Assess for malaria.
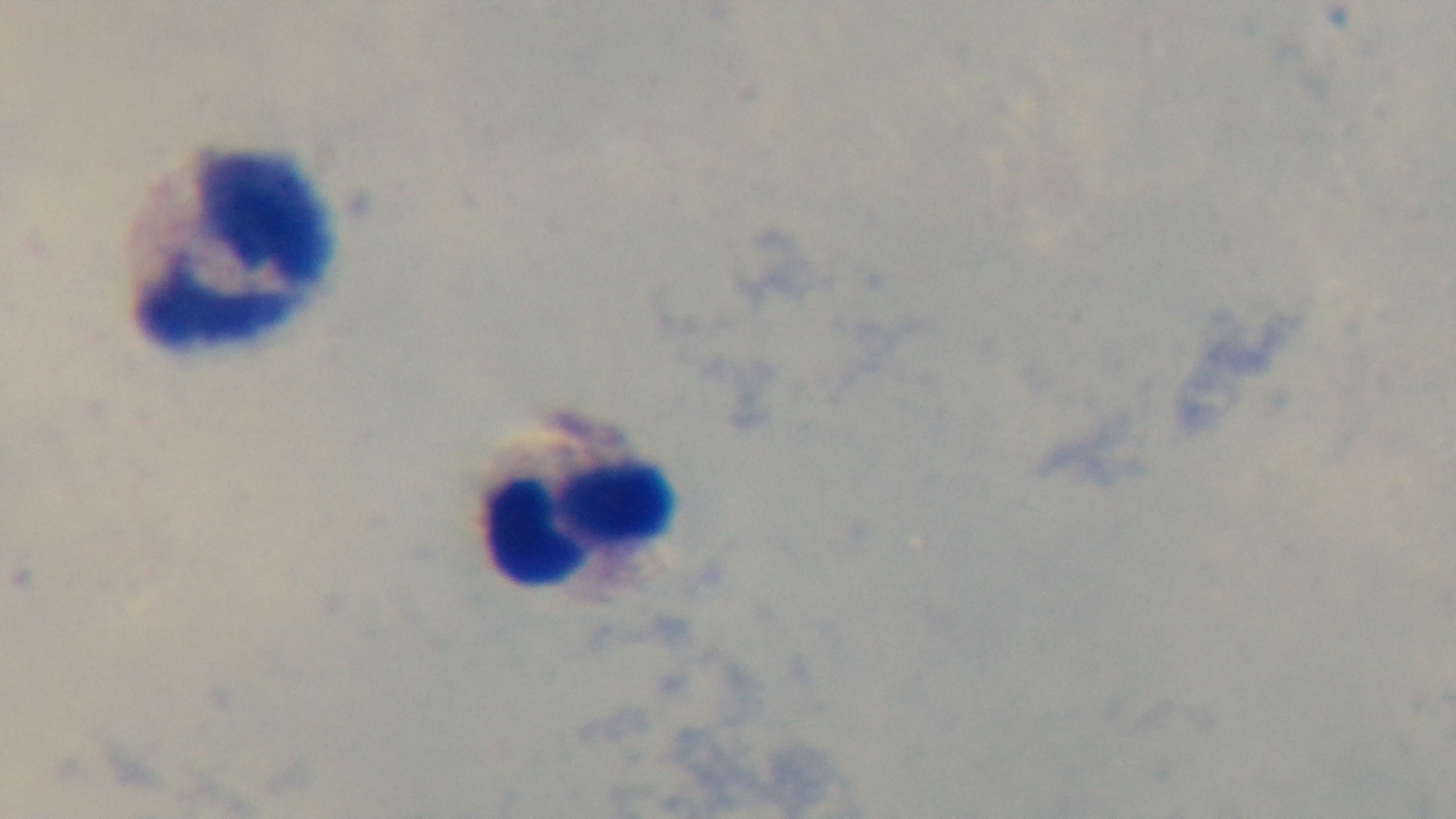

Negative.

Summary:
  - Preparation: thick blood film
  - Objective: 100x oil immersion
  - Modality: light microscopy
  - Capture: mounted 4K digital camera
  - Field of view: one from the slide
  - Stain: Giemsa